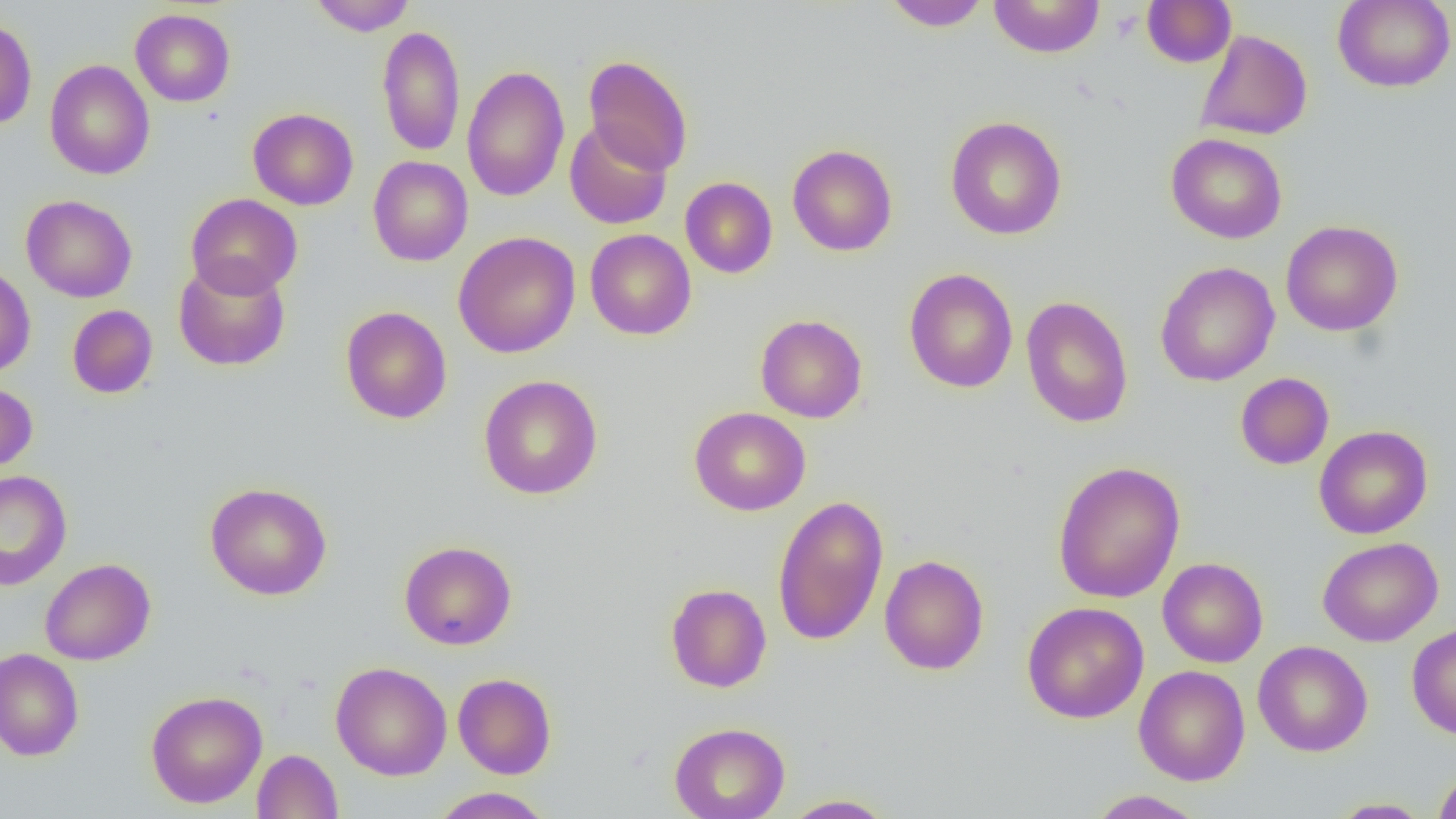
Summary:
  - Coordinate format: approximate bounding boxes as (x1,y1)-(x2,y2) corner pairs in pixels
  - Uninfected red blood cell locations: (309,0)-(417,35), (882,0)-(991,31), (988,0)-(1105,58), (1141,0)-(1236,68), (1332,0)-(1455,92), (130,8)-(235,106), (0,16)-(37,130), (377,25)-(465,157), (1195,29)-(1313,141), (583,54)-(694,175), (44,59)-(155,179), (462,65)-(570,202), (247,108)-(359,210), (945,116)-(1067,240), (563,120)-(672,230), (1166,133)-(1288,243), (787,144)-(898,256), (368,156)-(473,266), (680,177)-(777,278), (186,193)-(303,298), (21,194)-(137,303), (1280,220)-(1403,336), (585,229)-(696,340), (453,231)-(581,358), (172,258)-(291,371), (1155,261)-(1280,387), (0,265)-(36,378), (904,268)-(1018,393), (1021,296)-(1134,428), (67,305)-(158,399), (340,306)-(452,424), (755,314)-(868,423), (1235,372)-(1334,470), (478,375)-(603,499), (0,382)-(38,474), (689,406)-(811,516), (1314,425)-(1432,539), (1052,460)-(1186,604), (0,470)-(72,590), (205,482)-(332,600), (772,495)-(889,646), (1317,537)-(1443,647), (399,540)-(517,650), (879,555)-(989,675), (40,558)-(156,665), (1157,558)-(1268,667), (665,583)-(772,692), (1022,602)-(1149,723), (1407,623)-(1456,739), (1253,640)-(1373,757), (0,648)-(84,762), (331,661)-(451,780), (1134,665)-(1250,786), (452,673)-(557,779), (145,690)-(268,808), (669,722)-(790,819), (252,749)-(343,818), (1433,767)-(1456,819), (430,787)-(555,818), (1087,789)-(1207,818), (781,794)-(898,818), (1327,798)-(1433,818)
  - Slide-level diagnosis: negative for blood parasites
  - Preparation: thin blood smear
  - Modality: optical microscopy
  - Field of view: single
  - Magnification: 1000x
  - Image size: 1456×819 pixels